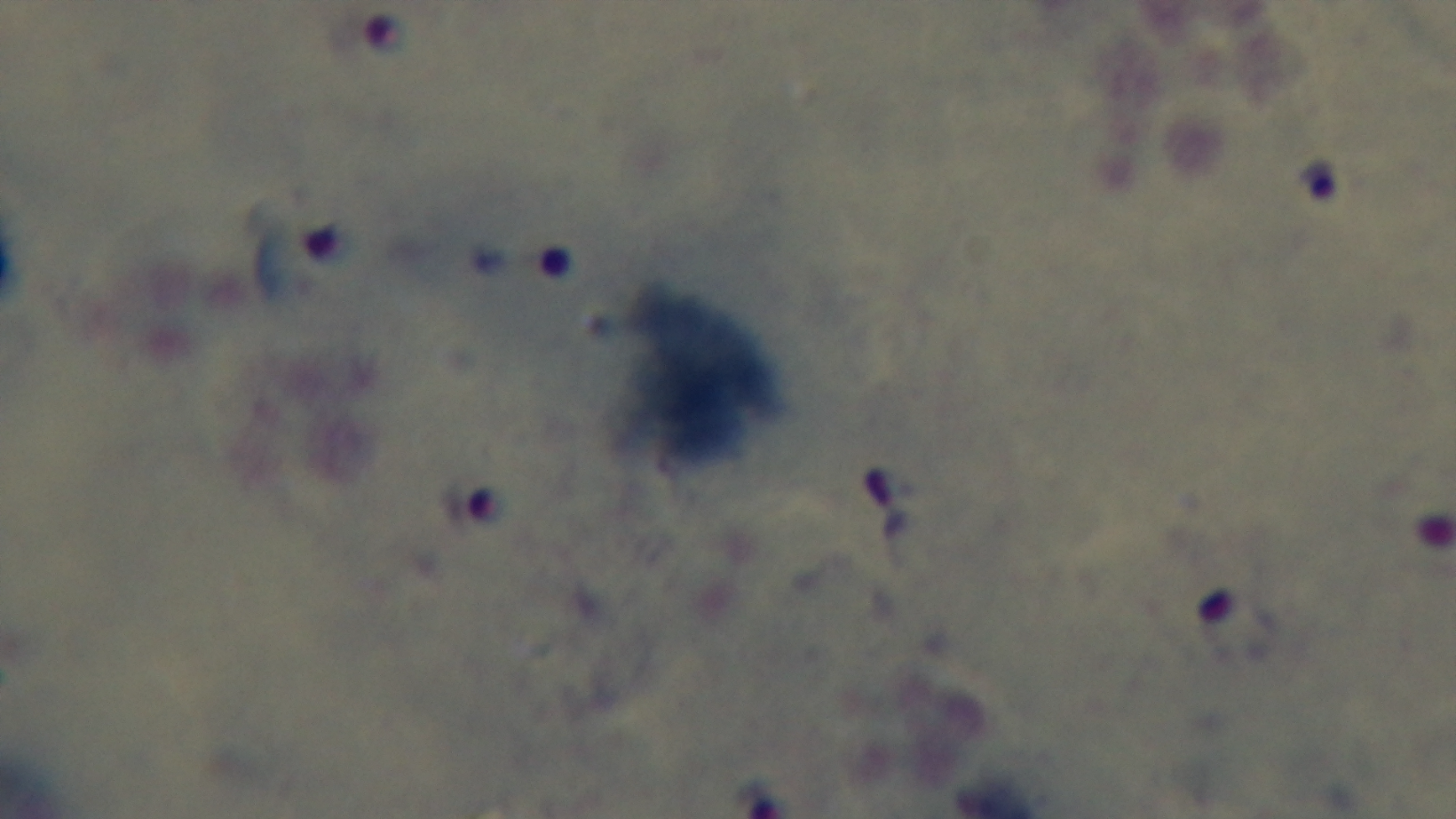

Mounted 4K digital camera. Photomicrograph. Malaria status: infected. Giemsa stain. Preparation: thick smear. Single field of view. 100x oil-immersion objective.